Assess this cell for malaria.
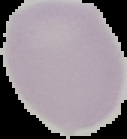
Uninfected.

Summary:
  - Image size: 127×139 pixels
  - Preparation: thin blood film
  - Image type: segmented cell region on a black background